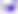

Summary:
  - Magnification: 400x
  - Identification: Toxoplasma gondii
  - Modality: micrograph